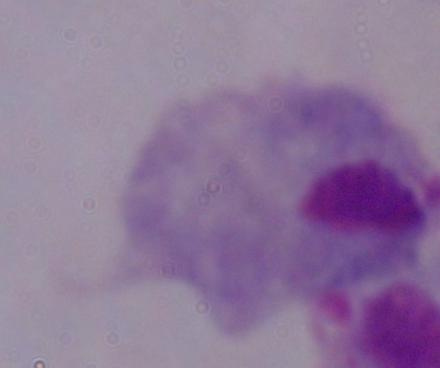

Summary:
  - Modality: micrograph
  - Identification: trichomonad
  - Magnification: 1000x